Identify the preparation type.
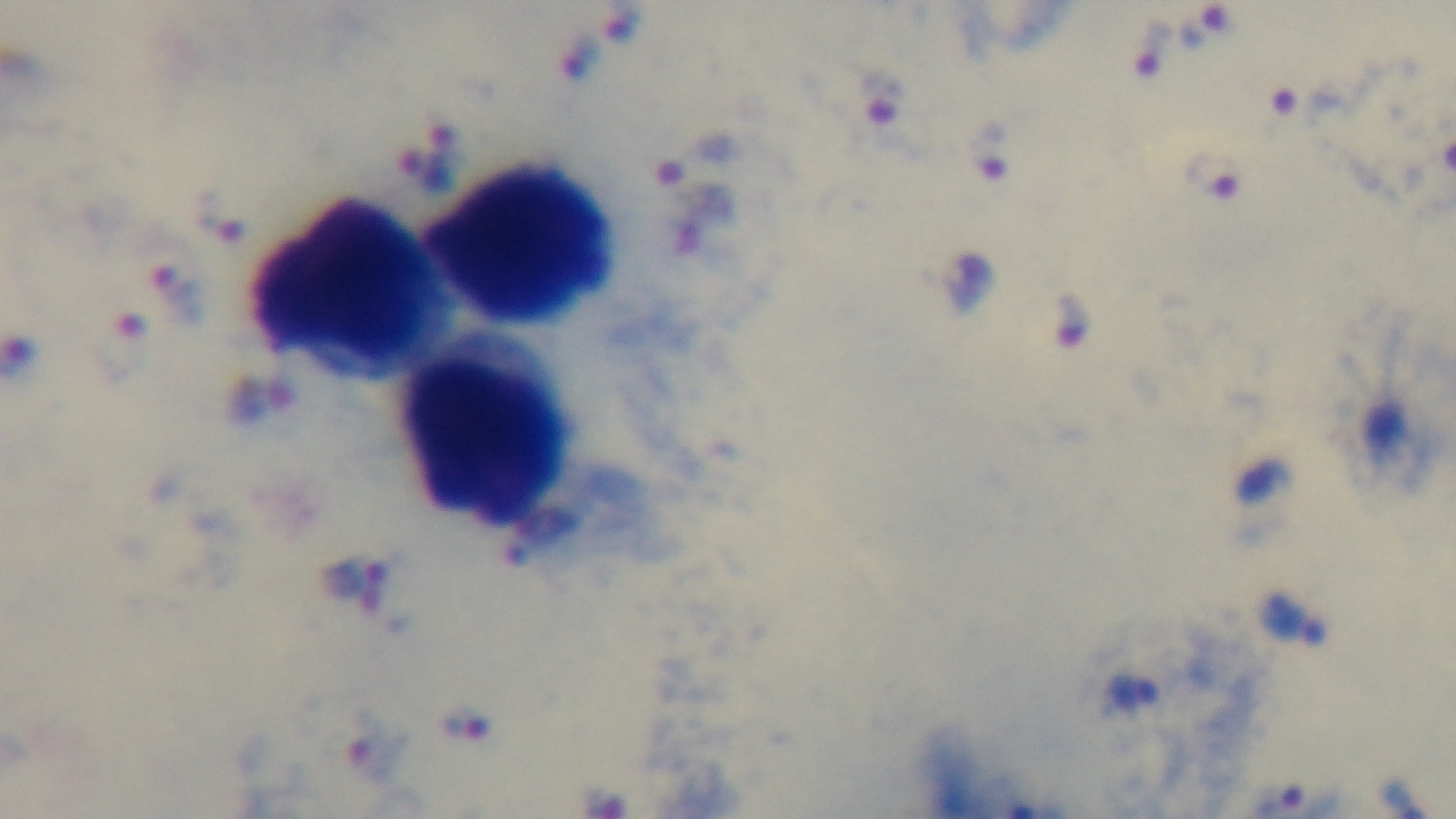
A thick smear.

Photomicrograph. Malaria status: infected. Oil-immersion objective, 100x. Giemsa stain. One field from the slide. Mounted 4K digital camera.